Classify this cell by malaria status.
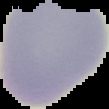
Parasitized.

preparation = thin blood smear
image size = 109×109 pixels
image type = segmented cell region with the area outside set to black